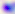

modality: micrograph
identification: Toxoplasma gondii
magnification: 400x